Comment on the morphology of the erythrocytes.
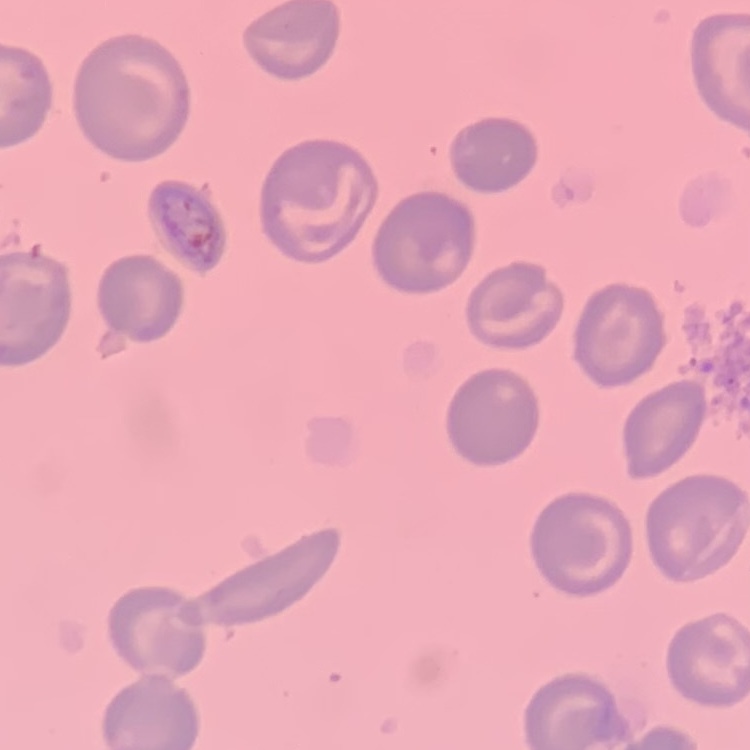

They show no rouleaux formation.

preparation: thin blood film
stain: Field's or Giemsa
image_type: square crop of a larger photomicrograph